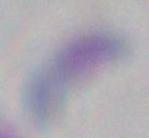
identification: Toxoplasma gondii
modality: photomicrograph
magnification: 1000x